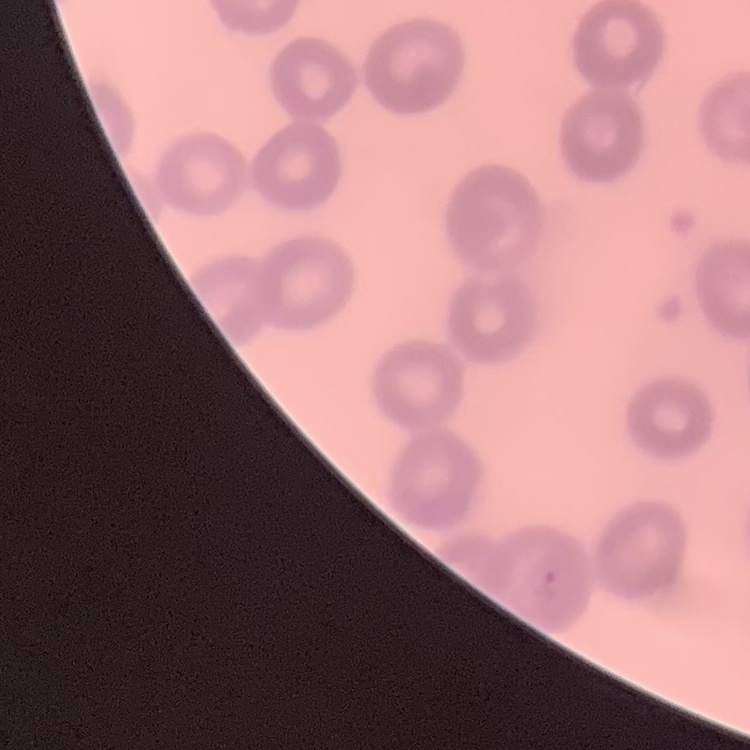
Summary:
  - Erythrocyte morphology: no rouleaux formation
  - Preparation: thin blood film
  - Stain: Field's or Giemsa
  - Image type: square crop of a larger photomicrograph